Assess this cell for malaria.
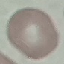
It is uninfected.

Summary:
  - Preparation: thin smear
  - Capture: smartphone through the microscope eyepiece
  - Stain: Giemsa
  - Image type: cell patch, automatically extracted from a larger field of view and resized to 64 × 64 pixels